Report the malaria status of this cell.
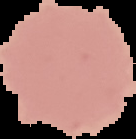
It is uninfected.

Summary:
  - Image size: 136×139 pixels
  - Image type: cell region segmented out of the field of view; surrounding area masked to black
  - Preparation: thin blood film